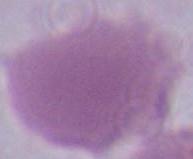

Summary:
  - Magnification: 1000x
  - Identification: erythrocyte
  - Modality: photomicrograph